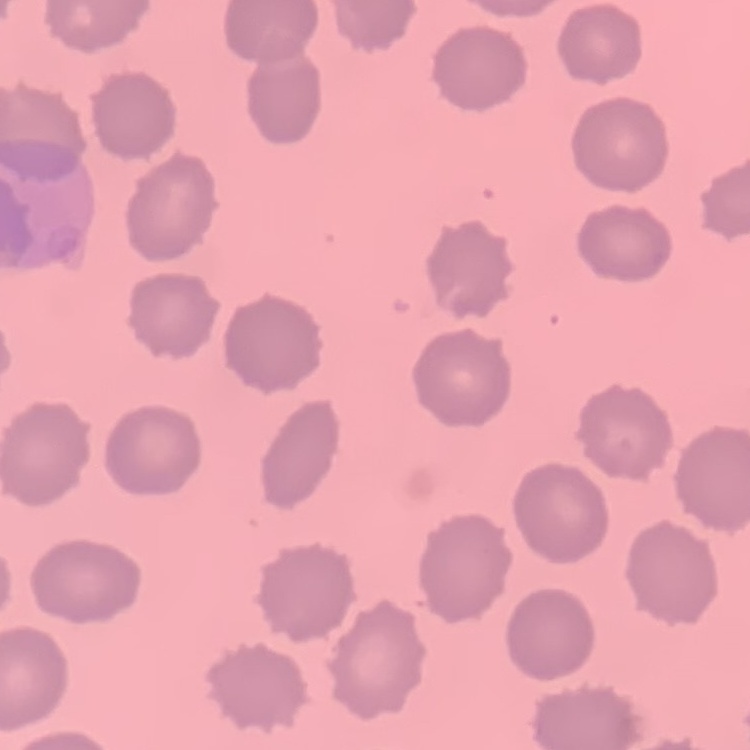

red blood cell morphology = no rouleaux formation
stain = Field's or Giemsa
image type = square crop of a larger photomicrograph
preparation = thin peripheral smear